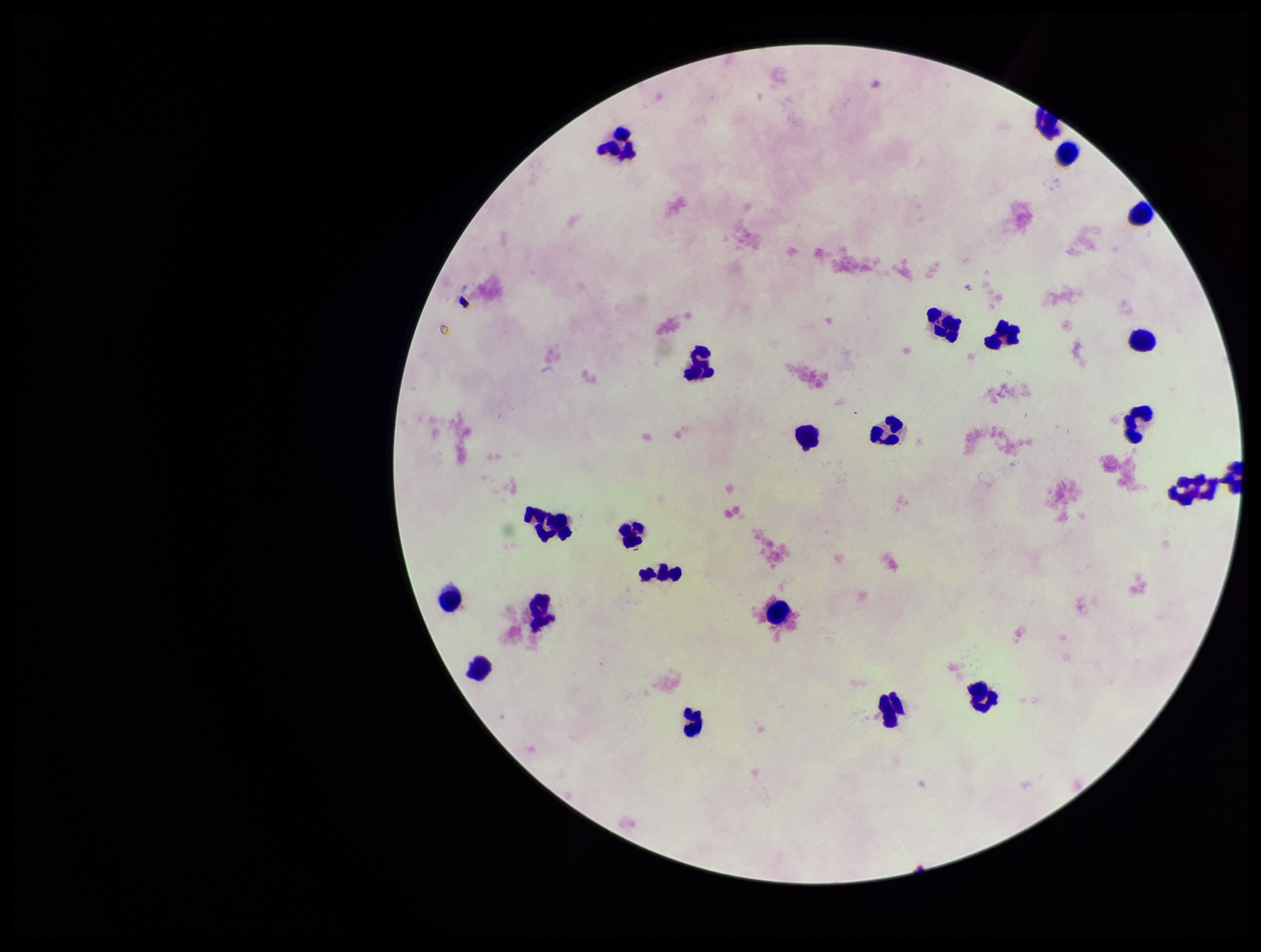
Summary:
  - Field of view: single
  - Leukocyte count: 22
  - Image size: 1261×952 pixels
  - Plasmodium parasites: none identified
  - Preparation: thick smear
  - Capture: smartphone photograph through the microscope eyepiece
  - Parasite count: 0
  - Stain: Giemsa
  - Patient malaria status: negative